Locate cells.
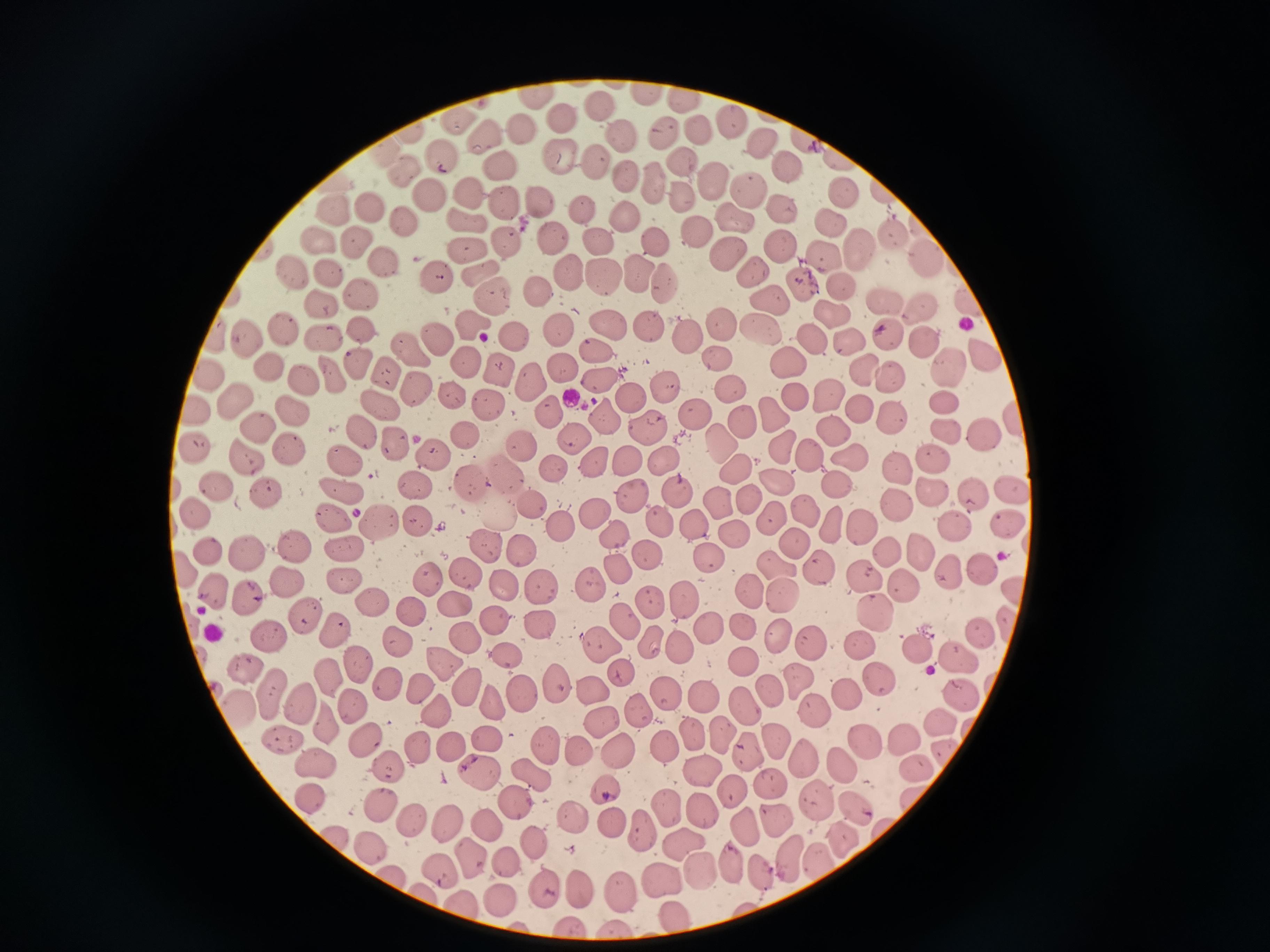

Approximate object centers, in pixels from the top-left corner.
Cells: (x=600, y=104), (x=729, y=123), (x=521, y=127), (x=702, y=132), (x=664, y=134), (x=480, y=136), (x=621, y=139), (x=759, y=142), (x=562, y=155), (x=442, y=156), (x=591, y=161), (x=689, y=167), (x=785, y=168), (x=502, y=170), (x=405, y=171), (x=625, y=174), (x=655, y=187), (x=715, y=190), (x=749, y=191), (x=467, y=195), (x=682, y=195), (x=428, y=196), (x=846, y=197), (x=539, y=202), (x=505, y=204), (x=371, y=207), (x=781, y=208), (x=336, y=211), (x=583, y=211), (x=627, y=218), (x=734, y=218), (x=403, y=219), (x=467, y=220), (x=832, y=220), (x=692, y=228), (x=552, y=237), (x=356, y=239), (x=894, y=241), (x=659, y=242), (x=469, y=243), (x=601, y=244), (x=509, y=245), (x=778, y=249), (x=861, y=250), (x=727, y=252), (x=822, y=260), (x=384, y=265), (x=481, y=268), (x=566, y=270), (x=327, y=273), (x=752, y=273), (x=637, y=276), (x=601, y=277), (x=440, y=280), (x=801, y=284), (x=664, y=285), (x=839, y=290), (x=538, y=291), (x=363, y=295), (x=489, y=297), (x=884, y=302), (x=773, y=303), (x=323, y=307), (x=922, y=308), (x=830, y=317), (x=720, y=321), (x=610, y=322), (x=471, y=324), (x=361, y=327), (x=758, y=328), (x=283, y=329), (x=652, y=329), (x=558, y=330), (x=435, y=335), (x=248, y=336), (x=511, y=336), (x=686, y=336), (x=890, y=337), (x=321, y=338), (x=850, y=340), (x=922, y=341), (x=813, y=345), (x=408, y=347), (x=600, y=354), (x=717, y=358), (x=984, y=359), (x=358, y=362), (x=469, y=362), (x=789, y=364), (x=948, y=368), (x=271, y=369), (x=564, y=369), (x=386, y=370), (x=503, y=370), (x=867, y=372), (x=332, y=374), (x=210, y=375), (x=537, y=381), (x=594, y=381), (x=892, y=381), (x=303, y=382), (x=661, y=383), (x=416, y=386), (x=726, y=387), (x=633, y=395), (x=829, y=397), (x=796, y=399), (x=234, y=400), (x=453, y=400), (x=379, y=402), (x=943, y=402), (x=485, y=406), (x=858, y=409), (x=550, y=410), (x=771, y=410), (x=198, y=411), (x=289, y=412), (x=693, y=414), (x=741, y=420), (x=889, y=420), (x=604, y=422), (x=648, y=427), (x=254, y=428), (x=949, y=433), (x=985, y=434), (x=358, y=436), (x=470, y=437), (x=834, y=437), (x=572, y=438), (x=714, y=439), (x=398, y=441), (x=781, y=444), (x=527, y=445), (x=199, y=449), (x=289, y=449), (x=431, y=453), (x=847, y=454), (x=246, y=455), (x=812, y=456), (x=666, y=460), (x=931, y=460), (x=349, y=461), (x=630, y=462), (x=594, y=464), (x=898, y=469), (x=554, y=470), (x=508, y=471), (x=737, y=471), (x=772, y=481), (x=472, y=484), (x=217, y=485), (x=340, y=486), (x=836, y=486), (x=415, y=487), (x=927, y=487), (x=265, y=491), (x=1011, y=491), (x=681, y=495), (x=974, y=497), (x=630, y=498), (x=749, y=502), (x=716, y=503), (x=894, y=504), (x=531, y=506), (x=802, y=508), (x=197, y=510), (x=595, y=513), (x=330, y=514), (x=503, y=516), (x=381, y=518), (x=772, y=519), (x=657, y=520), (x=834, y=521), (x=418, y=523), (x=860, y=523), (x=563, y=525), (x=956, y=526), (x=699, y=527), (x=1006, y=527), (x=734, y=533), (x=621, y=540), (x=487, y=541), (x=799, y=543), (x=343, y=545), (x=293, y=546), (x=523, y=549), (x=208, y=550), (x=918, y=550), (x=886, y=552), (x=247, y=553), (x=706, y=554), (x=650, y=558), (x=821, y=565), (x=773, y=567), (x=619, y=569), (x=946, y=570), (x=981, y=571), (x=862, y=573), (x=467, y=574), (x=426, y=577), (x=342, y=578), (x=285, y=581), (x=903, y=584), (x=539, y=585), (x=589, y=586), (x=503, y=589), (x=750, y=592), (x=215, y=595), (x=246, y=597), (x=681, y=599), (x=780, y=599), (x=648, y=602), (x=373, y=603), (x=453, y=603), (x=873, y=612), (x=413, y=613), (x=306, y=615), (x=626, y=619), (x=494, y=621), (x=540, y=623), (x=740, y=626), (x=706, y=627), (x=331, y=628), (x=978, y=633), (x=778, y=636), (x=272, y=638), (x=464, y=639), (x=396, y=640), (x=598, y=642), (x=856, y=642), (x=652, y=643), (x=809, y=643), (x=679, y=644), (x=913, y=649), (x=957, y=654), (x=509, y=660), (x=743, y=661), (x=439, y=663), (x=243, y=665), (x=360, y=665), (x=617, y=669), (x=330, y=678), (x=798, y=680), (x=880, y=682), (x=388, y=683), (x=468, y=687), (x=419, y=688), (x=558, y=690), (x=267, y=691), (x=592, y=691), (x=842, y=692), (x=772, y=693), (x=519, y=694), (x=666, y=694), (x=958, y=694), (x=701, y=695), (x=494, y=703), (x=299, y=704), (x=354, y=705), (x=746, y=707), (x=240, y=708), (x=437, y=713), (x=639, y=713), (x=810, y=713), (x=942, y=718), (x=325, y=721), (x=601, y=721), (x=692, y=732), (x=718, y=736), (x=489, y=738), (x=905, y=738), (x=284, y=739), (x=365, y=740), (x=775, y=741), (x=866, y=741), (x=451, y=745), (x=545, y=746), (x=419, y=747), (x=660, y=747), (x=751, y=748), (x=578, y=750), (x=618, y=750), (x=947, y=753), (x=806, y=755), (x=316, y=759), (x=842, y=763), (x=918, y=768), (x=698, y=769), (x=391, y=770), (x=480, y=771), (x=531, y=776), (x=773, y=785), (x=605, y=786), (x=735, y=792), (x=817, y=797), (x=311, y=798), (x=916, y=799), (x=513, y=802), (x=854, y=805), (x=380, y=806), (x=670, y=807), (x=702, y=810), (x=577, y=816), (x=778, y=816), (x=411, y=818), (x=447, y=820), (x=483, y=826), (x=617, y=826), (x=749, y=829), (x=647, y=830), (x=335, y=839), (x=678, y=842), (x=541, y=843), (x=369, y=847), (x=819, y=857), (x=790, y=859), (x=473, y=860), (x=509, y=862), (x=731, y=864), (x=701, y=870), (x=760, y=871), (x=442, y=873), (x=662, y=879), (x=397, y=883), (x=581, y=885), (x=619, y=888), (x=548, y=889), (x=428, y=896), (x=499, y=899), (x=461, y=907), (x=673, y=919), (x=567, y=925), (x=613, y=929).

Thin smear of blood. Single field of view. Acquired by smartphone through the microscope eyepiece. Image is 1270×952 pixels. Giemsa stain.